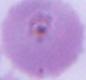
Summary:
  - Modality: micrograph
  - Magnification: 1000x
  - Identification: red blood cell